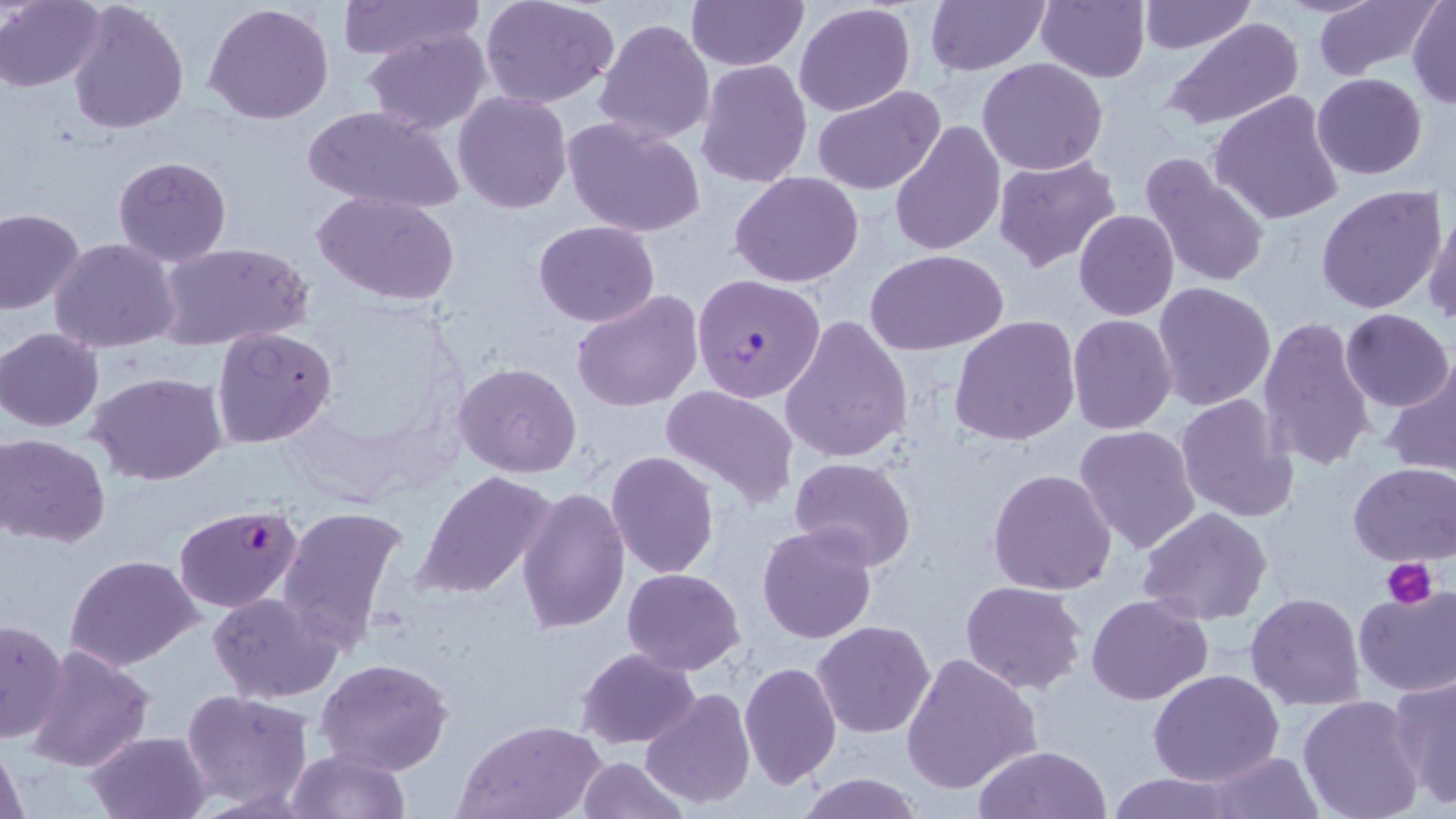 Approximate bounding boxes as (x1, y1, x2, y2) in pixels. Plasmodium falciparum-infected red blood cell locations: (692, 273, 825, 402), (174, 503, 305, 612). Uninfected red blood cell locations: (67, 0, 190, 136), (339, 0, 484, 60), (480, 0, 622, 109), (686, 0, 807, 70), (924, 0, 1052, 75), (1035, 0, 1151, 84), (1138, 0, 1255, 54), (1314, 0, 1437, 81), (1407, 0, 1456, 109), (0, 1, 105, 91), (203, 2, 335, 124), (794, 2, 917, 117), (594, 16, 715, 144), (1162, 18, 1305, 133), (361, 29, 493, 133), (977, 57, 1108, 176), (696, 59, 811, 188), (1311, 73, 1428, 180), (812, 86, 948, 195), (452, 90, 573, 213), (1209, 90, 1346, 227), (301, 104, 465, 214), (563, 116, 706, 238), (887, 119, 1006, 257), (992, 153, 1121, 271), (1138, 153, 1274, 291), (113, 155, 233, 266), (730, 172, 864, 288), (1315, 184, 1448, 315), (312, 191, 460, 306), (1424, 202, 1456, 329), (0, 208, 85, 314), (1074, 210, 1180, 321), (533, 220, 659, 327), (49, 238, 181, 354), (156, 243, 313, 351), (865, 249, 1009, 356), (1151, 281, 1276, 411), (571, 288, 703, 411), (1340, 308, 1454, 412), (779, 314, 914, 464), (1066, 314, 1179, 437), (948, 315, 1081, 447), (1257, 315, 1380, 473), (212, 326, 337, 449), (1, 327, 104, 431), (1379, 360, 1456, 477), (453, 363, 582, 478), (86, 370, 227, 487), (661, 384, 799, 510), (1174, 392, 1300, 525), (1073, 424, 1203, 555), (2, 432, 112, 546), (606, 451, 719, 577), (789, 457, 916, 571), (1347, 461, 1456, 566), (414, 468, 559, 600), (986, 468, 1117, 595), (517, 487, 629, 634), (277, 503, 410, 650), (1138, 508, 1275, 625), (756, 522, 879, 645), (64, 554, 204, 672), (622, 567, 746, 675), (960, 579, 1089, 696), (1353, 586, 1456, 696), (209, 591, 341, 704), (1245, 592, 1365, 711), (1087, 594, 1214, 706), (0, 618, 70, 743), (811, 620, 936, 739), (24, 643, 155, 773), (575, 647, 701, 749), (900, 650, 1043, 795), (315, 657, 455, 775), (739, 661, 843, 789), (1148, 670, 1284, 788), (1390, 673, 1456, 810), (641, 687, 755, 810), (181, 689, 313, 809), (1297, 694, 1425, 819), (455, 718, 608, 819), (85, 728, 214, 819), (1, 740, 30, 819), (972, 745, 1114, 819), (285, 747, 410, 818), (1201, 749, 1326, 818), (576, 756, 689, 818), (794, 774, 927, 818), (1102, 774, 1240, 819). Platelet locations: (1382, 558, 1438, 607). Slide-level diagnosis: Plasmodium falciparum. Single field of view. May-Grünwald-Giemsa-stained preparation. Light microscopy. Image is 1456×819 pixels. 1000x magnification. Thin blood film.